Comment on the morphology of the red blood cells.
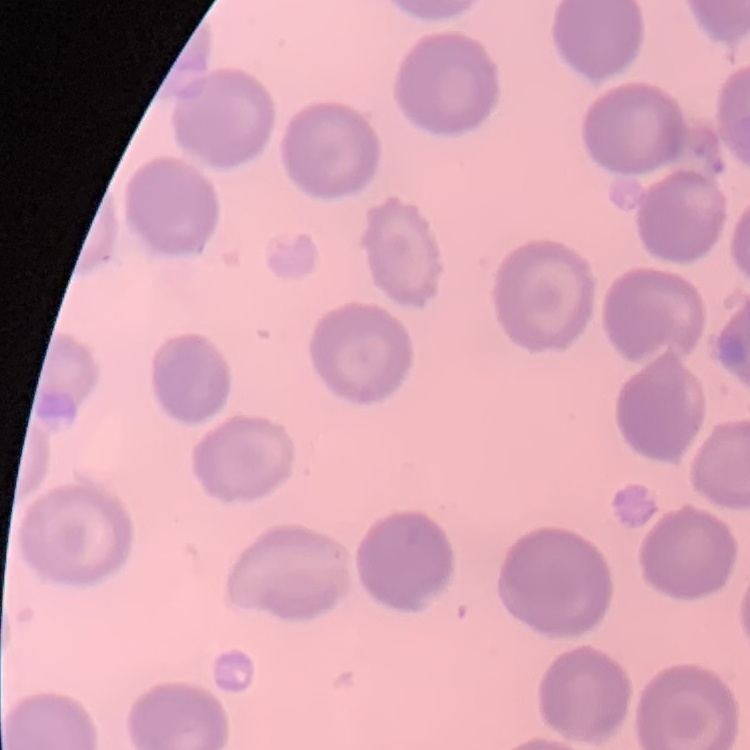
No rouleaux formation.

Square crop of a larger photomicrograph. Thin blood film. Stained with either Field's or Giemsa.